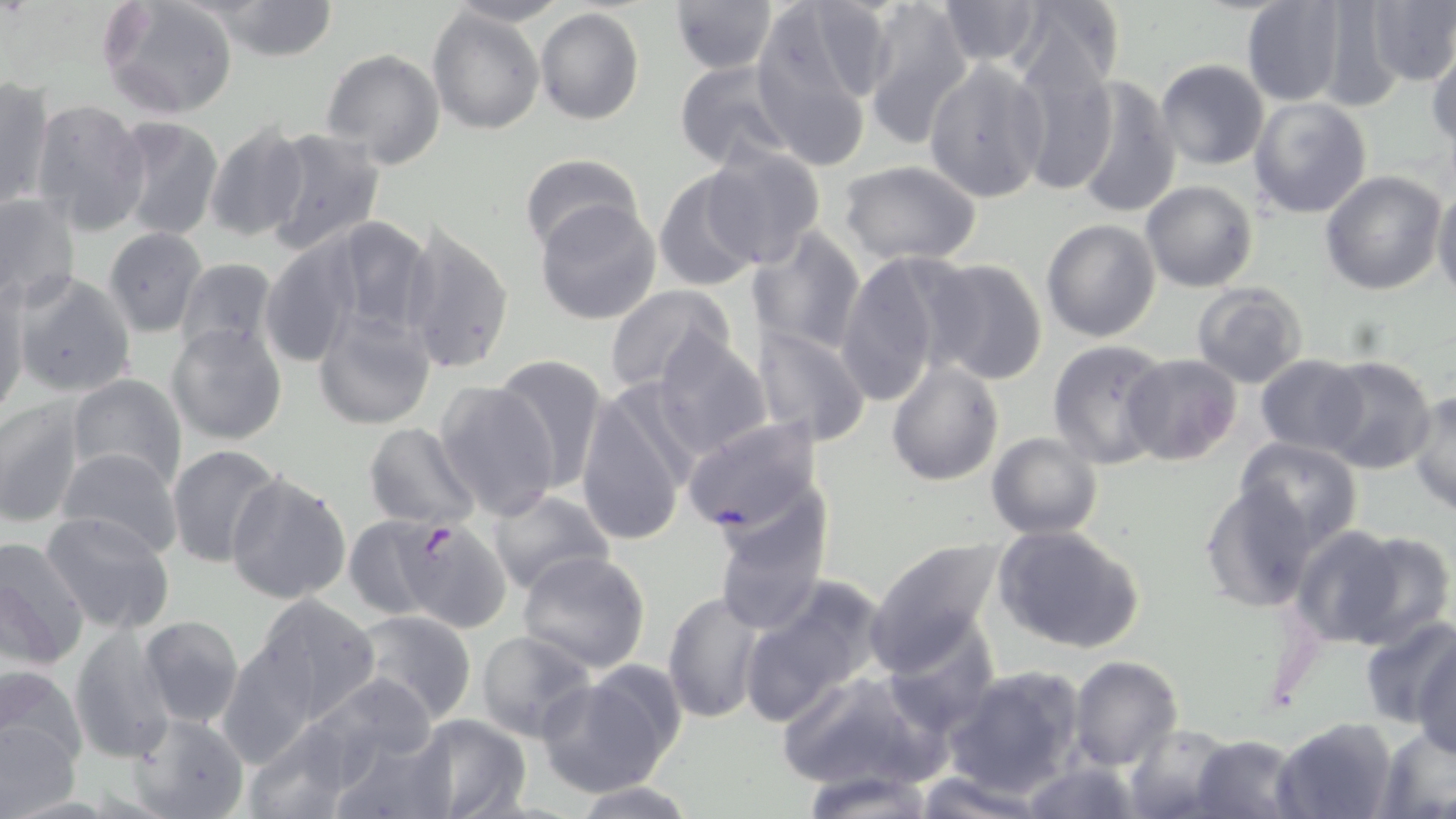
Summary:
  - Coordinate format: approximate bounding boxes as (x1, y1, x2, y2) in pixels
  - Uninfected red blood cell locations: (99, 0, 240, 120), (195, 0, 345, 62), (440, 0, 569, 27), (855, 0, 976, 143), (931, 0, 1054, 71), (1009, 0, 1125, 94), (1308, 0, 1412, 113), (1364, 0, 1456, 87), (667, 1, 779, 75), (1240, 1, 1348, 106), (428, 8, 544, 134), (535, 8, 644, 126), (736, 9, 885, 157), (878, 29, 1019, 186), (1427, 43, 1456, 152), (1009, 48, 1117, 197), (320, 49, 446, 170), (672, 58, 798, 169), (923, 59, 1050, 203), (1155, 59, 1269, 169), (1067, 74, 1181, 220), (0, 77, 53, 212), (1248, 95, 1372, 218), (30, 97, 151, 236), (111, 115, 224, 241), (201, 120, 314, 243), (258, 127, 388, 256), (701, 143, 827, 270), (518, 153, 645, 256), (837, 159, 984, 266), (653, 167, 766, 291), (1319, 170, 1447, 295), (1141, 180, 1258, 292), (1432, 184, 1456, 299), (0, 193, 79, 310), (535, 199, 661, 325), (316, 214, 438, 344), (1041, 217, 1161, 341), (399, 219, 514, 377), (747, 224, 868, 354), (102, 228, 209, 338), (260, 236, 362, 369), (837, 250, 955, 407), (175, 257, 281, 364), (919, 258, 1049, 386), (11, 271, 138, 398), (1190, 283, 1309, 388), (603, 284, 737, 394), (1, 285, 28, 421), (312, 305, 437, 429), (168, 324, 286, 446), (751, 324, 871, 448), (651, 330, 772, 461), (1048, 339, 1173, 469), (1121, 352, 1242, 466), (492, 354, 610, 488), (1255, 354, 1369, 455), (1314, 356, 1438, 475), (886, 359, 1003, 485), (65, 374, 186, 490), (434, 379, 560, 520), (576, 385, 692, 546), (1409, 391, 1456, 515), (0, 397, 86, 528), (681, 414, 825, 538), (363, 422, 480, 530), (987, 432, 1103, 540), (1235, 436, 1362, 550), (166, 444, 284, 567), (55, 446, 184, 560), (224, 472, 353, 605), (1259, 479, 1408, 631), (1198, 480, 1319, 613), (488, 488, 613, 596), (709, 497, 831, 635), (40, 512, 176, 634), (343, 514, 452, 621), (991, 523, 1147, 654), (1291, 525, 1441, 649), (867, 536, 1004, 672), (0, 537, 91, 667), (518, 550, 652, 674), (738, 576, 887, 725), (663, 589, 766, 724), (249, 594, 380, 721), (350, 610, 477, 723), (138, 615, 245, 729), (1357, 619, 1456, 731), (878, 624, 995, 739), (1410, 625, 1456, 758), (68, 626, 177, 758), (475, 631, 599, 743), (1068, 655, 1182, 772), (0, 664, 88, 778), (942, 664, 1085, 796), (538, 669, 678, 797), (775, 670, 942, 790), (305, 672, 441, 781), (127, 710, 249, 818), (0, 712, 80, 817), (404, 712, 531, 819), (1272, 716, 1399, 819), (241, 718, 370, 819), (1123, 724, 1238, 819), (1374, 728, 1456, 816), (326, 732, 452, 818), (1190, 735, 1305, 819), (1015, 760, 1142, 819), (800, 770, 936, 817), (911, 772, 1045, 818), (566, 780, 703, 818)
  - Plasmodium falciparum-infected red blood cell locations: (401, 519, 511, 634)
  - Slide-level diagnosis: Plasmodium falciparum
  - Stain: May-Grünwald-Giemsa
  - Preparation: thin blood film
  - Image size: 1456×819 pixels
  - Magnification: 1000x
  - Modality: light microscopy
  - Field of view: one of a larger specimen